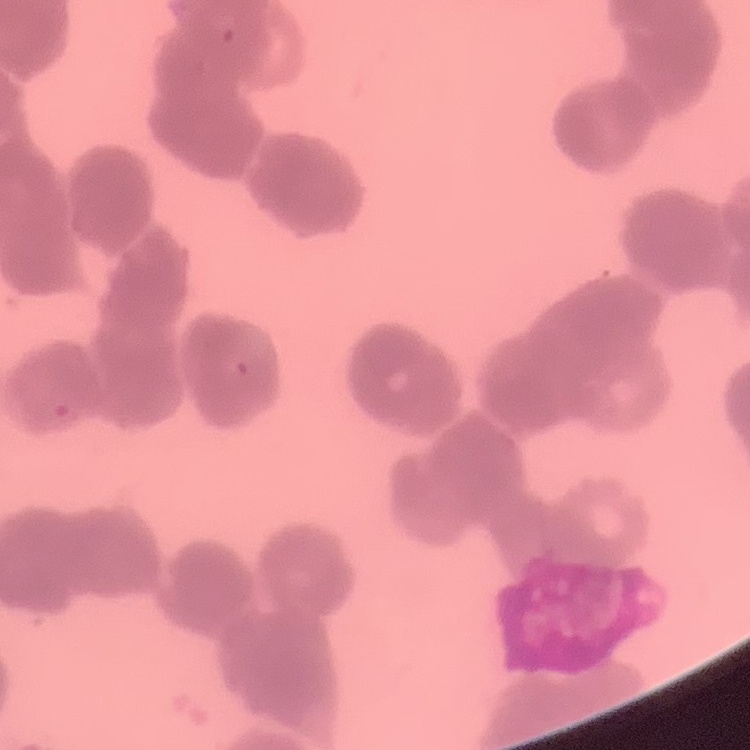
Summary:
  - Red blood cell morphology: rouleaux formation
  - Image type: one tile cut from a larger photomicrograph
  - Stain: Field's or Giemsa
  - Preparation: thin peripheral smear